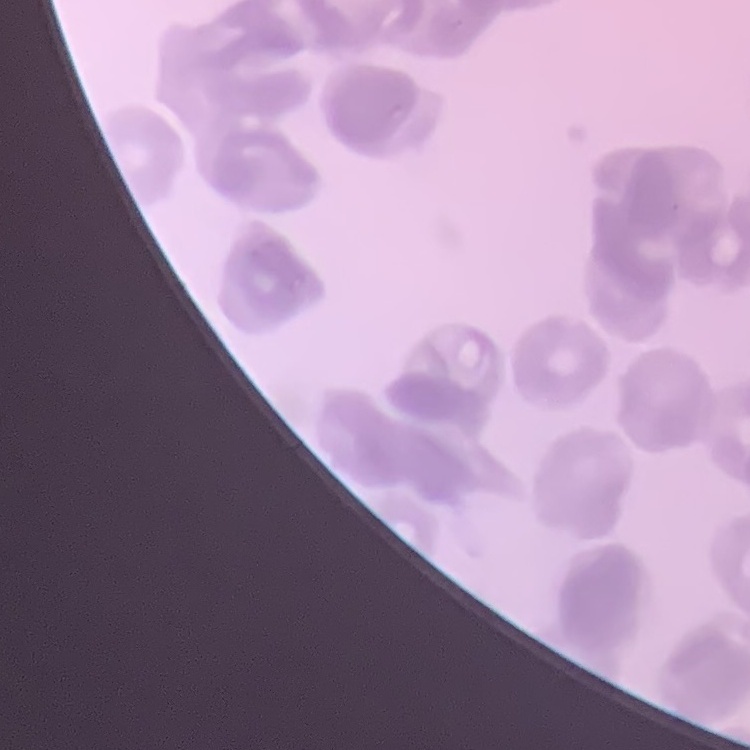

erythrocyte morphology = rouleaux formation
stain = Field's or Giemsa
image type = one tile cut from a larger photomicrograph
preparation = thin blood film